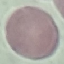

Result: no malaria parasites detected. Cell patch, automatically extracted from a larger field of view and resized to 64 × 64 pixels. Thin smear of blood. Photographed with a smartphone camera at the microscope eyepiece. Giemsa stain.